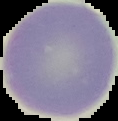

preparation = thin blood smear
image size = 118×121 pixels
image type = segmented cell region with the area outside set to black
result = no malaria parasites seen